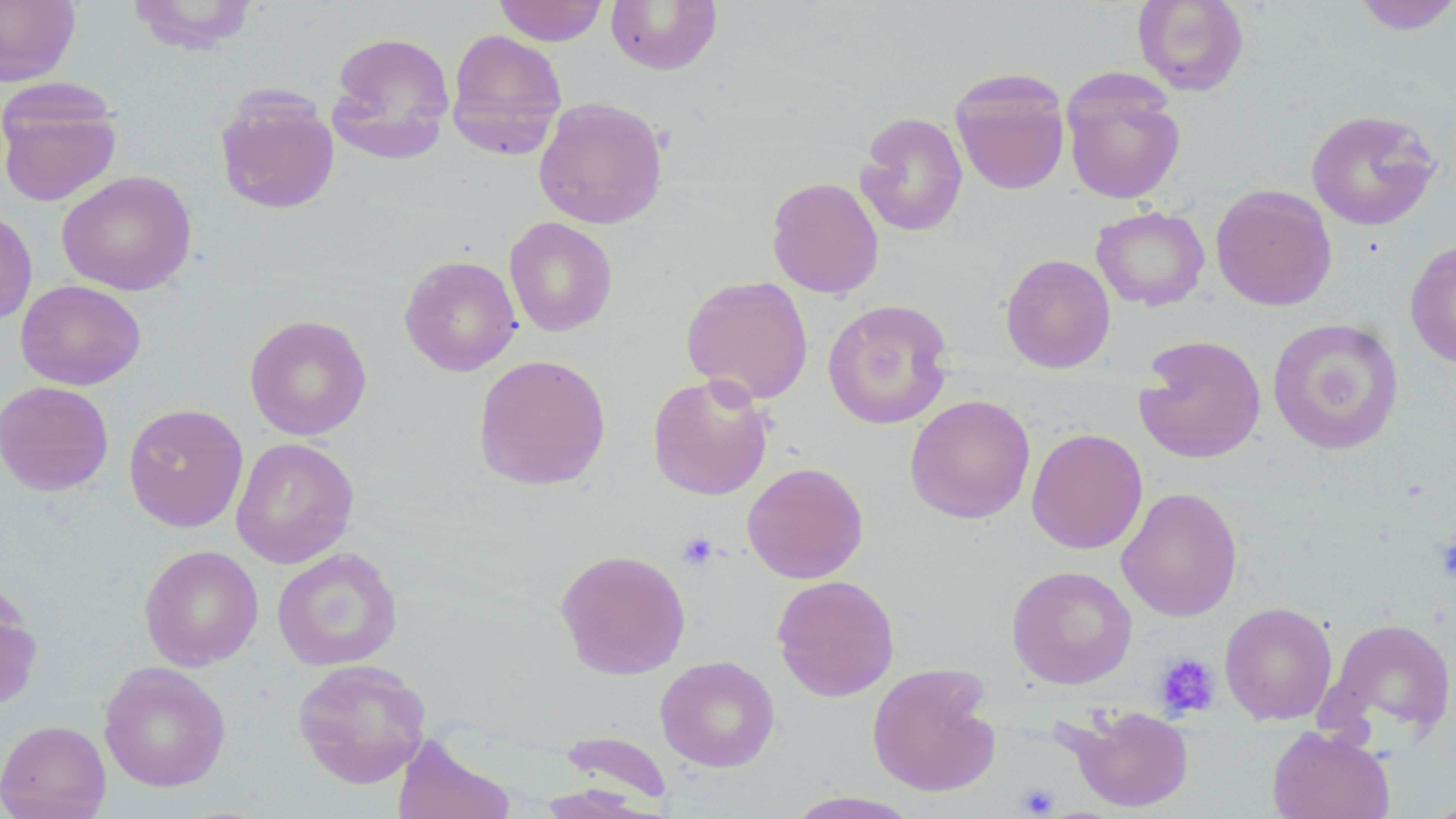

Summary:
  - Coordinate format: approximate bounding boxes as (x1,y1)-(x2,y2) corner pairs in pixels
  - Uninfected red blood cell locations: (0,0)-(80,86), (125,0)-(260,55), (493,0)-(609,46), (1133,0)-(1249,96), (1350,0)-(1456,35), (605,1)-(722,75), (445,28)-(567,158), (328,30)-(456,160), (950,67)-(1071,196), (1062,75)-(1186,205), (0,85)-(123,207), (215,89)-(340,215), (533,96)-(669,229), (1305,109)-(1441,231), (855,111)-(968,237), (56,170)-(196,296), (766,176)-(884,299), (1210,184)-(1337,311), (1091,205)-(1210,311), (0,209)-(37,326), (503,217)-(618,336), (1404,238)-(1456,369), (1000,253)-(1116,373), (398,255)-(522,377), (681,275)-(813,404), (15,279)-(146,390), (823,299)-(954,429), (244,314)-(372,441), (1267,317)-(1404,455), (1134,334)-(1267,464), (472,353)-(612,491), (647,373)-(774,501), (0,380)-(114,496), (905,394)-(1036,524), (123,403)-(248,532), (1026,428)-(1148,554), (231,437)-(359,568), (742,461)-(869,583), (761,463)-(881,701), (1116,487)-(1243,622), (139,544)-(264,671), (272,546)-(402,671), (555,548)-(691,680), (1007,564)-(1137,689), (771,574)-(900,701), (1220,602)-(1338,724), (1321,616)-(1456,744), (655,655)-(780,772), (292,658)-(432,788), (98,661)-(232,792), (867,662)-(1002,797), (1062,705)-(1195,813), (0,719)-(111,819), (1267,725)-(1395,819), (558,729)-(674,807), (392,734)-(515,819), (783,790)-(925,819)
  - Platelet locations: (677,531)-(719,570), (1433,533)-(1456,583), (1154,652)-(1220,717), (1017,783)-(1059,817)
  - Slide-level diagnosis: no evidence of blood parasites
  - Magnification: 1000x
  - Preparation: thin blood smear
  - Stain: May-Grünwald-Giemsa
  - Field of view: one of a larger specimen
  - Image size: 1456×819 pixels
  - Modality: optical microscopy